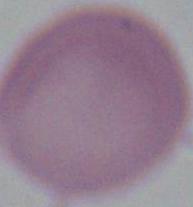
Summary:
  - Identification: red blood cell
  - Modality: photomicrograph
  - Magnification: 1000x